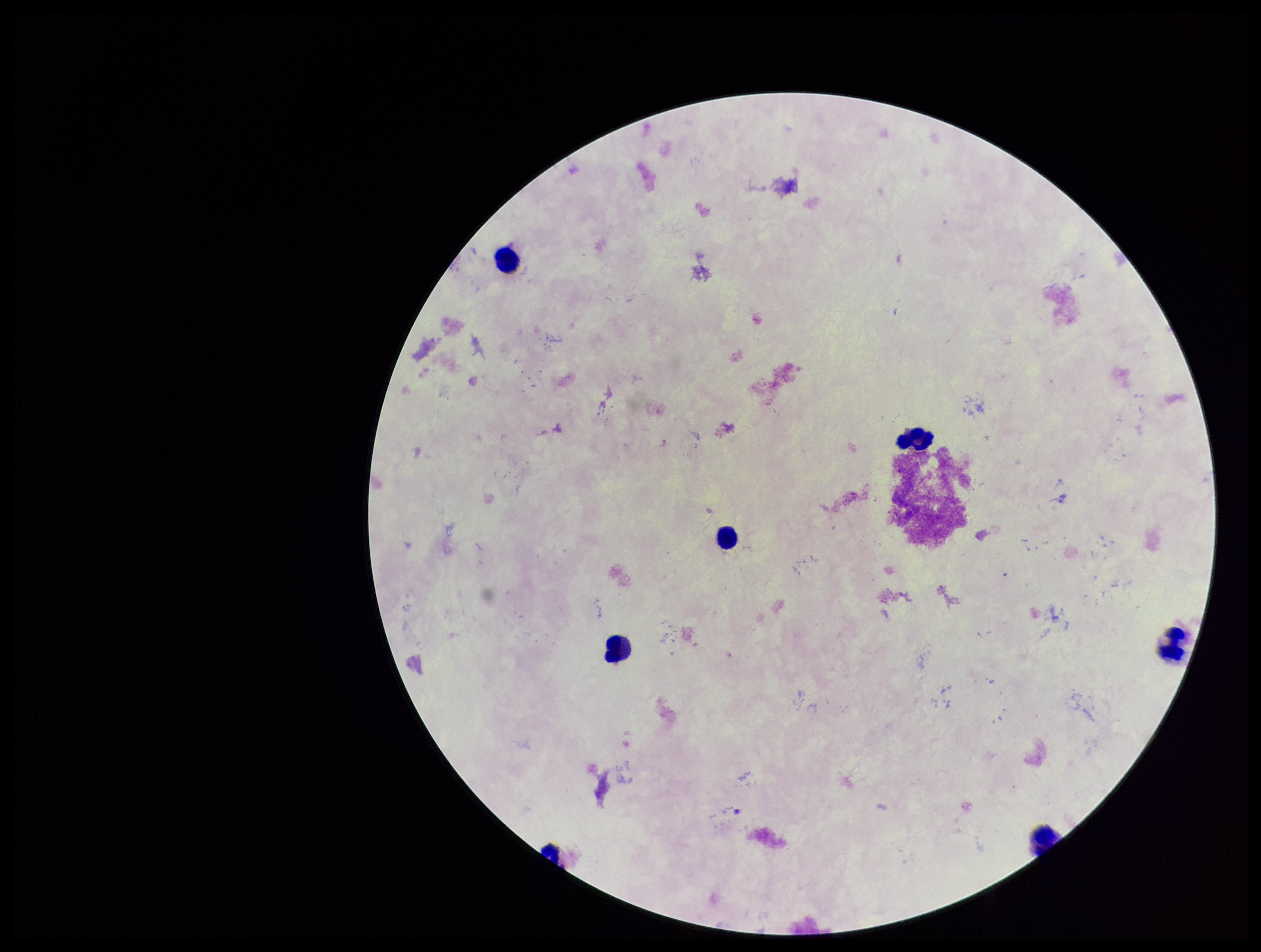
Leukocyte count: 6. Smartphone photograph taken through the eyepiece of a microscope. Giemsa stain. Preparation: thick. Parasite count: 0. Single field of view. Image is 1261×952 pixels. Plasmodium parasites: none detected. Patient malaria status: negative.